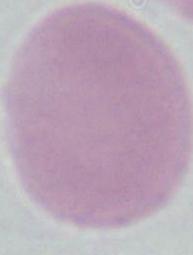
Summary:
  - Identification: red blood cell
  - Magnification: 1000x
  - Modality: micrograph